Assess this cell for malaria.
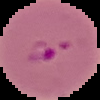

It is parasitized.

Summary:
  - Image type: cell region segmented out of the field of view; surrounding area masked to black
  - Preparation: thin blood smear
  - Image size: 100×100 pixels